Classify this cell by malaria status.
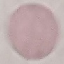

Uninfected.

Summary:
  - Capture: smartphone camera at the microscope eyepiece
  - Image type: automatically extracted cell patch, resized to 64 × 64 pixels
  - Stain: Giemsa
  - Preparation: thin blood smear